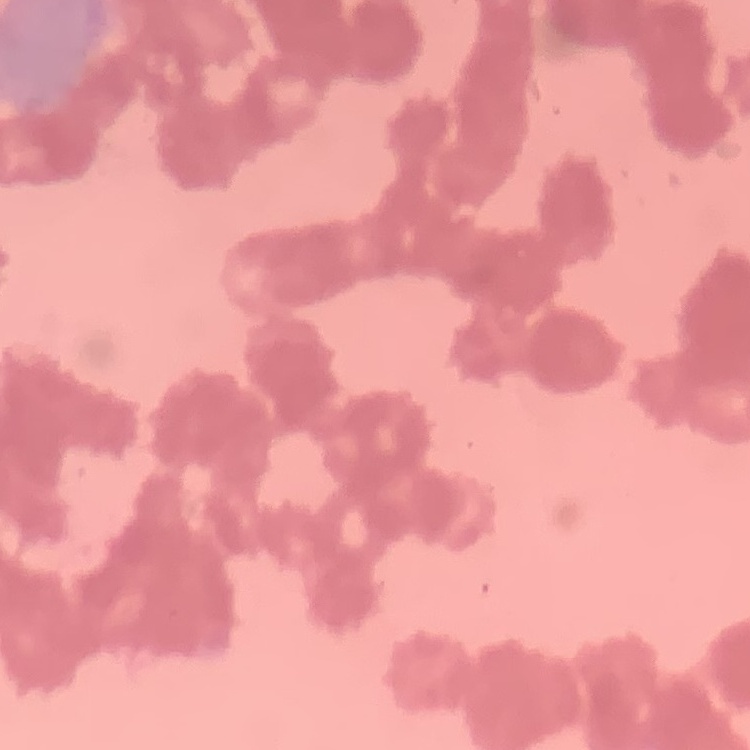

red blood cell morphology = rouleaux formation
image type = square crop of a larger photomicrograph
stain = Field's or Giemsa
preparation = thin peripheral smear